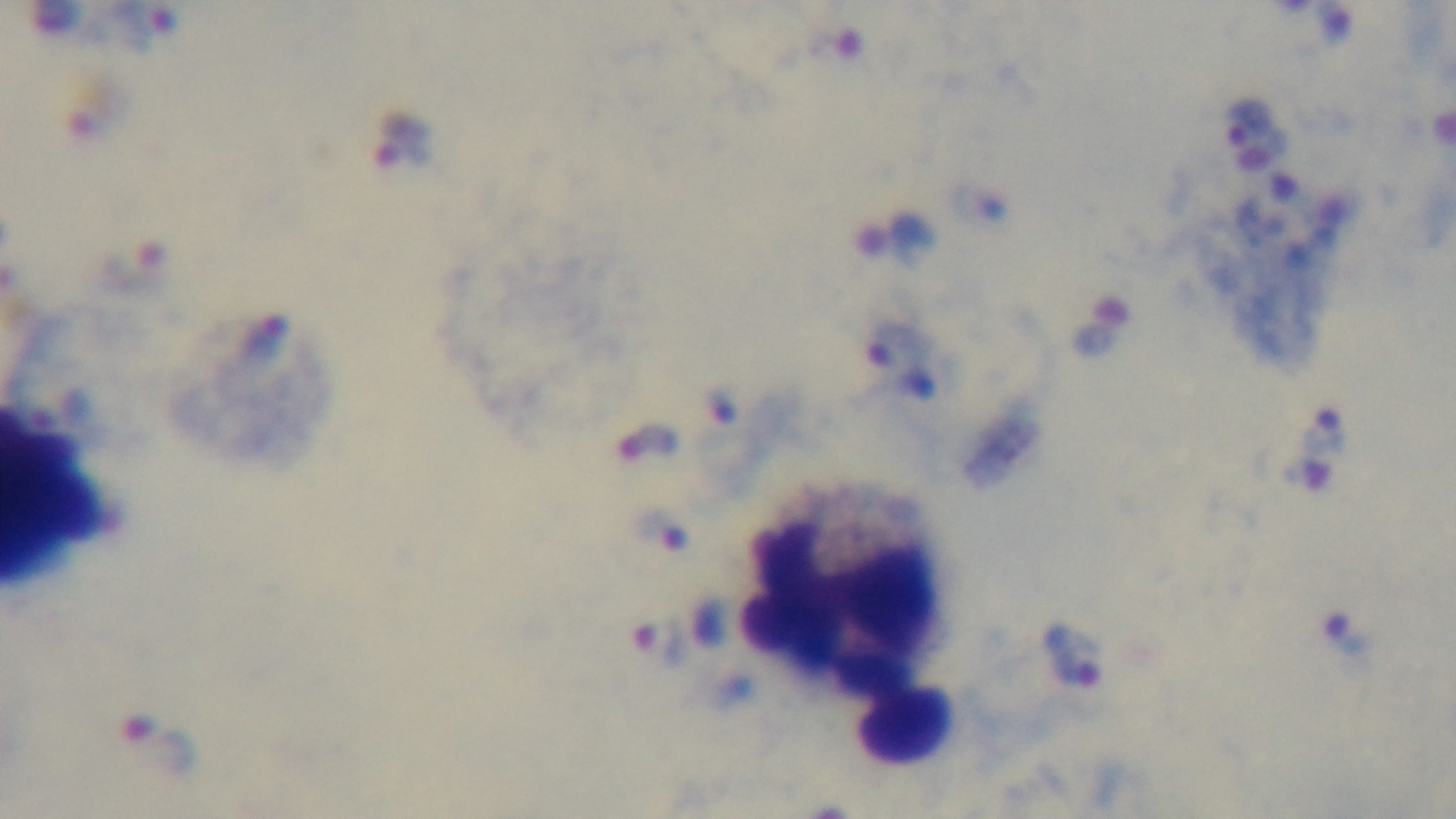
Summary:
  - Preparation: thick
  - Modality: light microscopy
  - Stain: Giemsa
  - Malaria status: infected
  - Field of view: single
  - Objective: 100x oil immersion
  - Capture: mounted 4K digital camera